Look for Plasmodium parasites.
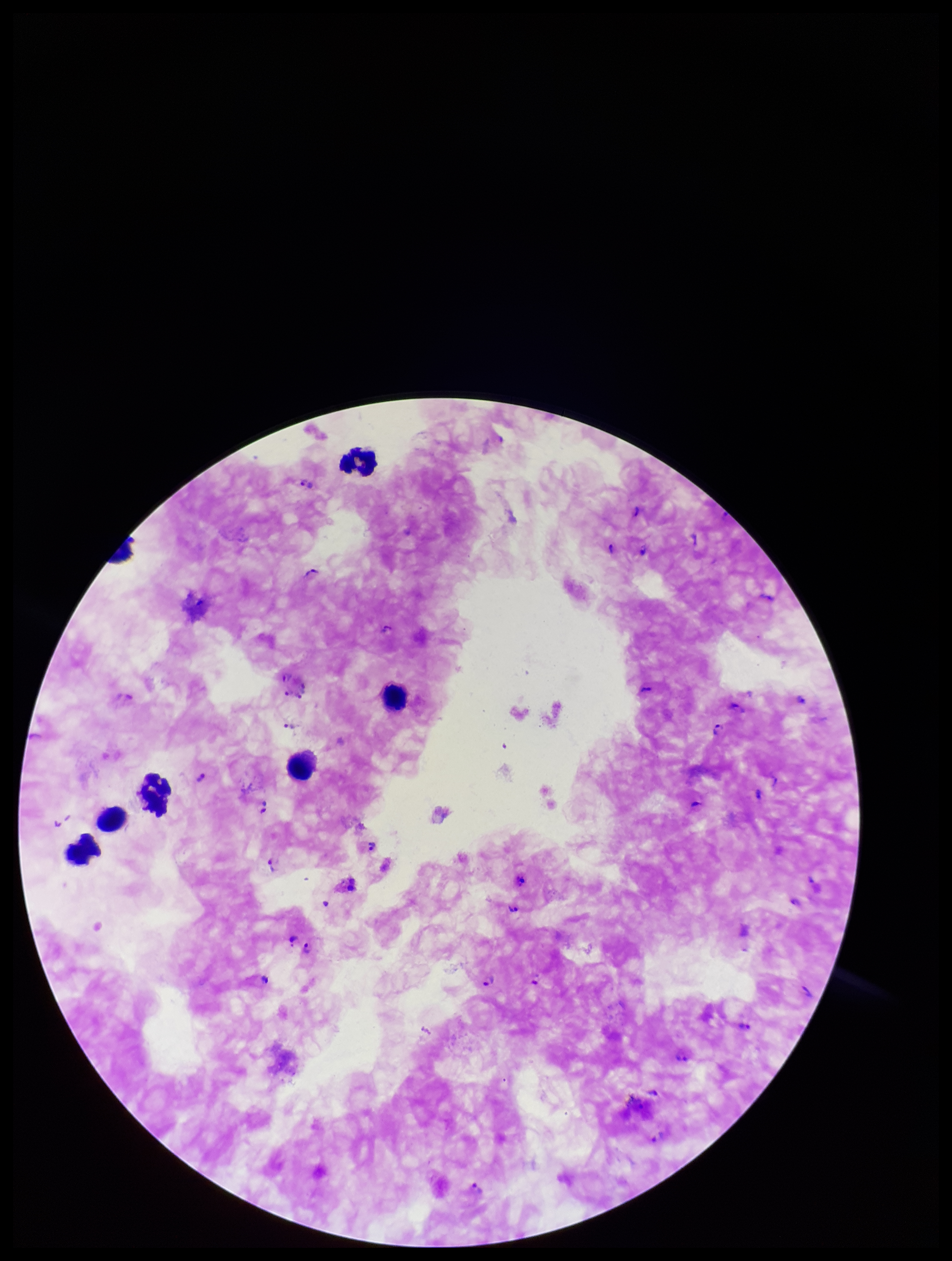

Identified.

Summary:
  - Species reported for this patient: Plasmodium falciparum
  - Image size: 952×1261 pixels
  - Field of view: one from this slide
  - Preparation: thick blood smear
  - Stain: Giemsa
  - Patient malaria status: positive
  - Parasite count: 23
  - Capture: smartphone photograph through the microscope eyepiece
  - Leukocyte count: 7